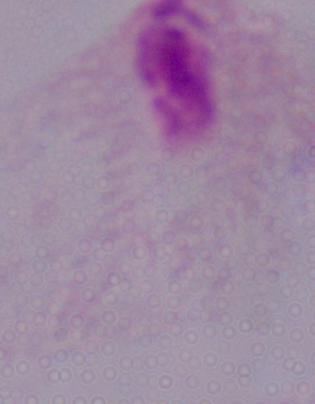
Captured at 1000x magnification. Photomicrograph. A trichomonad is seen.